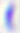 Captured at 400x magnification. Micrograph. Toxoplasma gondii is seen.